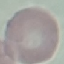

Summary:
  - Malaria status: uninfected
  - Stain: Giemsa
  - Image type: automatically extracted cell patch, resized to 64 × 64 pixels
  - Preparation: thin blood film
  - Capture: smartphone camera at the microscope eyepiece